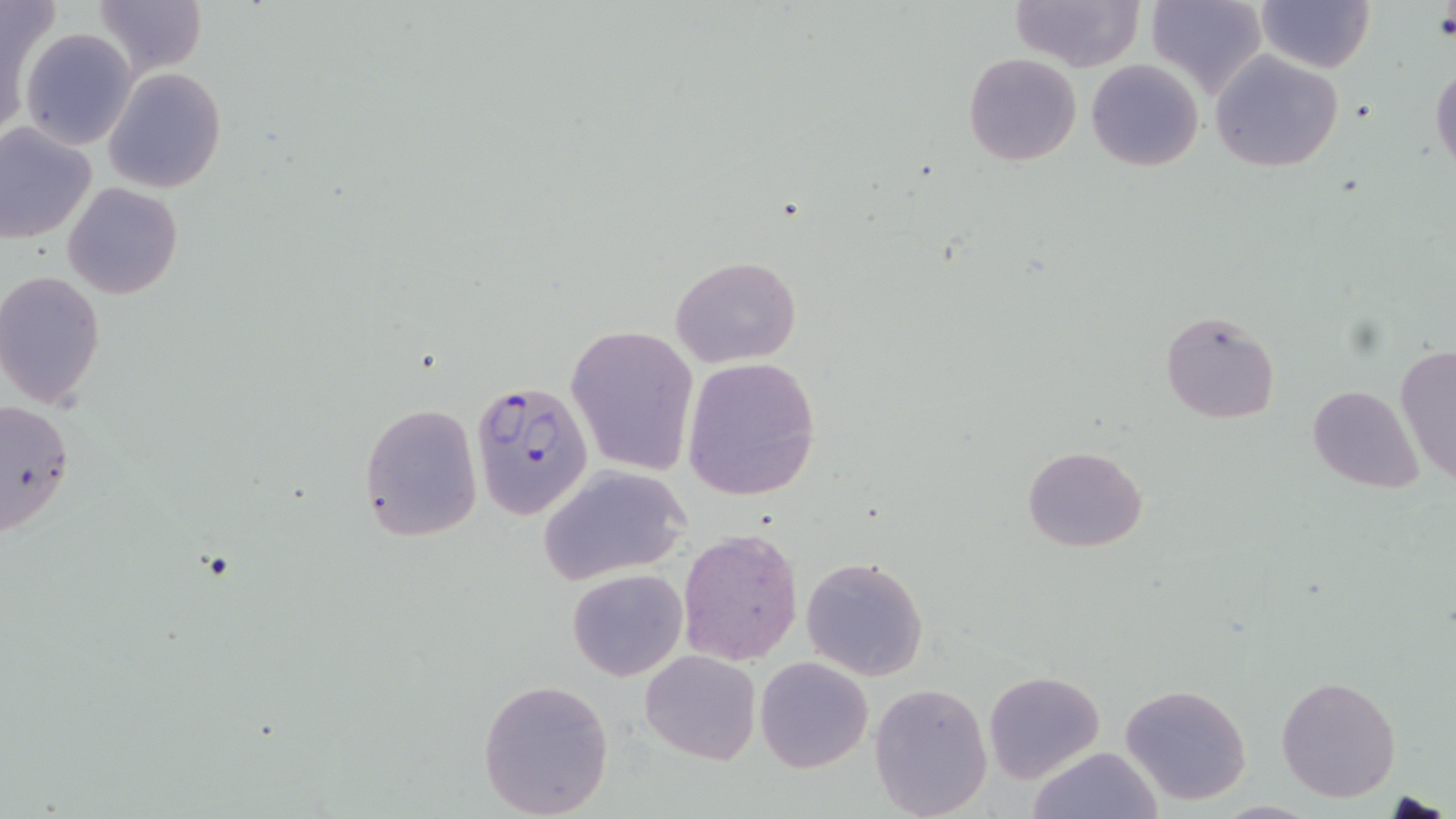
Approximate bounding boxes as (x1, y1, x2, y2) in pixels. Plasmodium falciparum-infected red blood cell locations: (470, 381, 594, 519). Uninfected red blood cell locations: (1010, 0, 1144, 71), (1145, 0, 1268, 100), (92, 1, 208, 78), (1257, 1, 1374, 73), (2, 6, 43, 136), (18, 28, 138, 150), (1208, 50, 1345, 172), (964, 53, 1081, 167), (1086, 60, 1203, 171), (1431, 61, 1455, 174), (103, 66, 228, 193), (0, 121, 97, 245), (64, 182, 183, 299), (671, 256, 801, 369), (0, 271, 105, 409), (1160, 310, 1282, 424), (567, 323, 699, 477), (1394, 345, 1456, 486), (681, 358, 820, 501), (1308, 385, 1425, 492), (0, 397, 74, 539), (359, 402, 484, 544), (1022, 445, 1149, 552), (540, 465, 691, 582), (678, 528, 804, 665), (800, 557, 929, 681), (567, 568, 688, 681), (640, 650, 761, 765), (754, 656, 873, 773), (983, 671, 1106, 783), (1276, 675, 1402, 803), (478, 677, 615, 818), (869, 681, 994, 817), (1119, 682, 1253, 806), (1026, 746, 1164, 819), (1384, 792, 1448, 817). Slide-level diagnosis: Plasmodium falciparum. Single field of view. Image is 1456×819 pixels. Thin blood smear. May-Grünwald-Giemsa stain. 1000x magnification. Light microscopy.